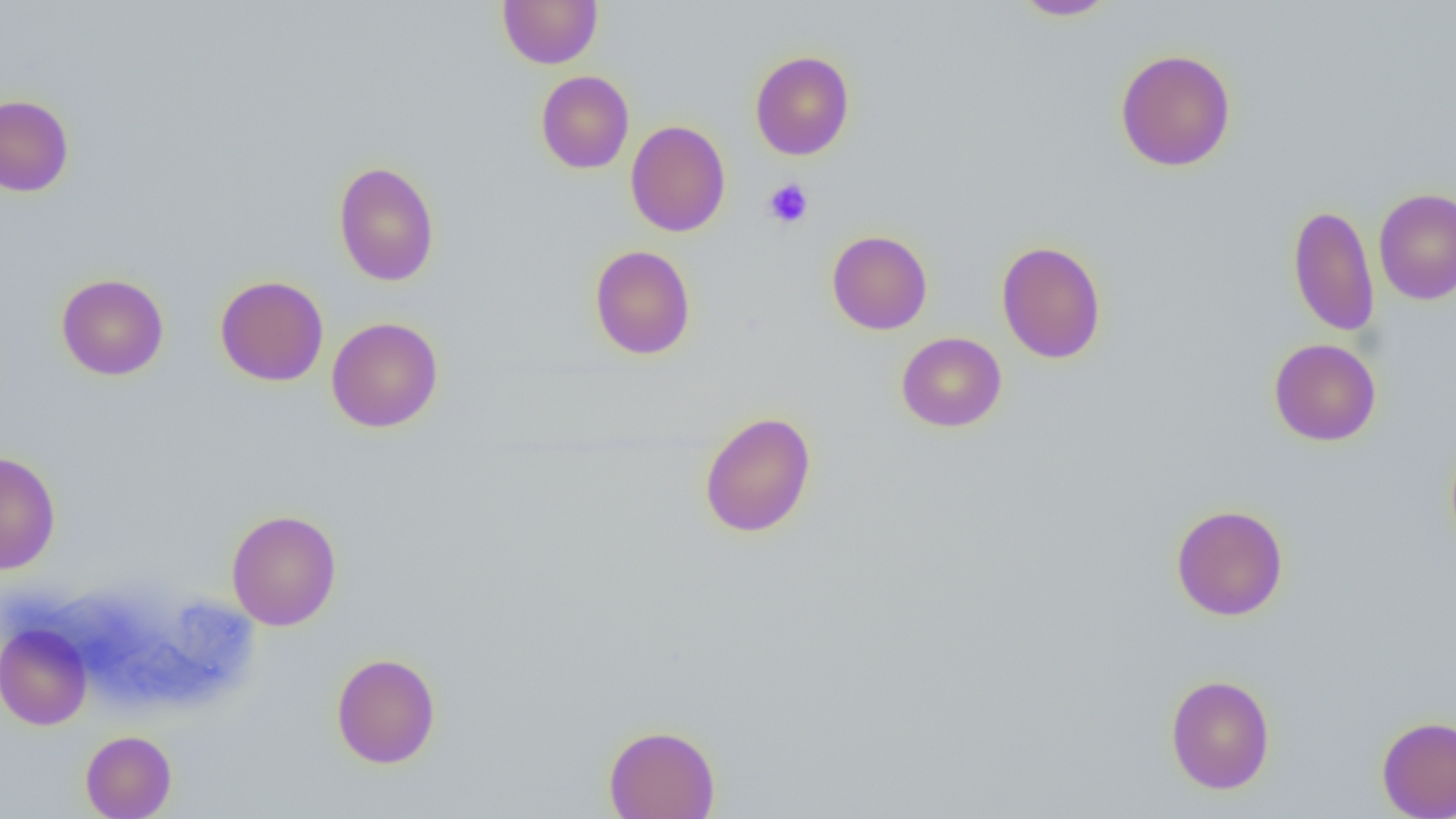

Summary:
  - Coordinate format: approximate bounding boxes as (x1, y1, x2, y2) in pixels
  - Platelet locations: (762, 179, 814, 228)
  - Uninfected red blood cell locations: (497, 0, 603, 68), (1011, 0, 1118, 20), (1115, 48, 1236, 172), (749, 50, 855, 160), (535, 70, 634, 174), (0, 94, 74, 197), (625, 120, 730, 237), (333, 161, 440, 287), (1373, 188, 1456, 305), (1287, 204, 1379, 337), (826, 229, 933, 335), (995, 240, 1107, 364), (589, 245, 696, 360), (56, 273, 169, 380), (215, 275, 329, 387), (326, 317, 444, 433), (896, 331, 1007, 432), (1268, 338, 1381, 446), (699, 410, 816, 539), (0, 451, 61, 574), (1170, 503, 1289, 621), (226, 509, 342, 631), (0, 623, 92, 730), (331, 652, 441, 768), (1165, 674, 1276, 794), (1377, 715, 1456, 819), (604, 724, 721, 819), (80, 730, 176, 819)
  - Slide-level diagnosis: negative for blood parasites
  - Magnification: 1000x
  - Field of view: one of a larger specimen
  - Modality: optical microscopy
  - Image size: 1456×819 pixels
  - Preparation: thin blood smear